Identify the preparation type.
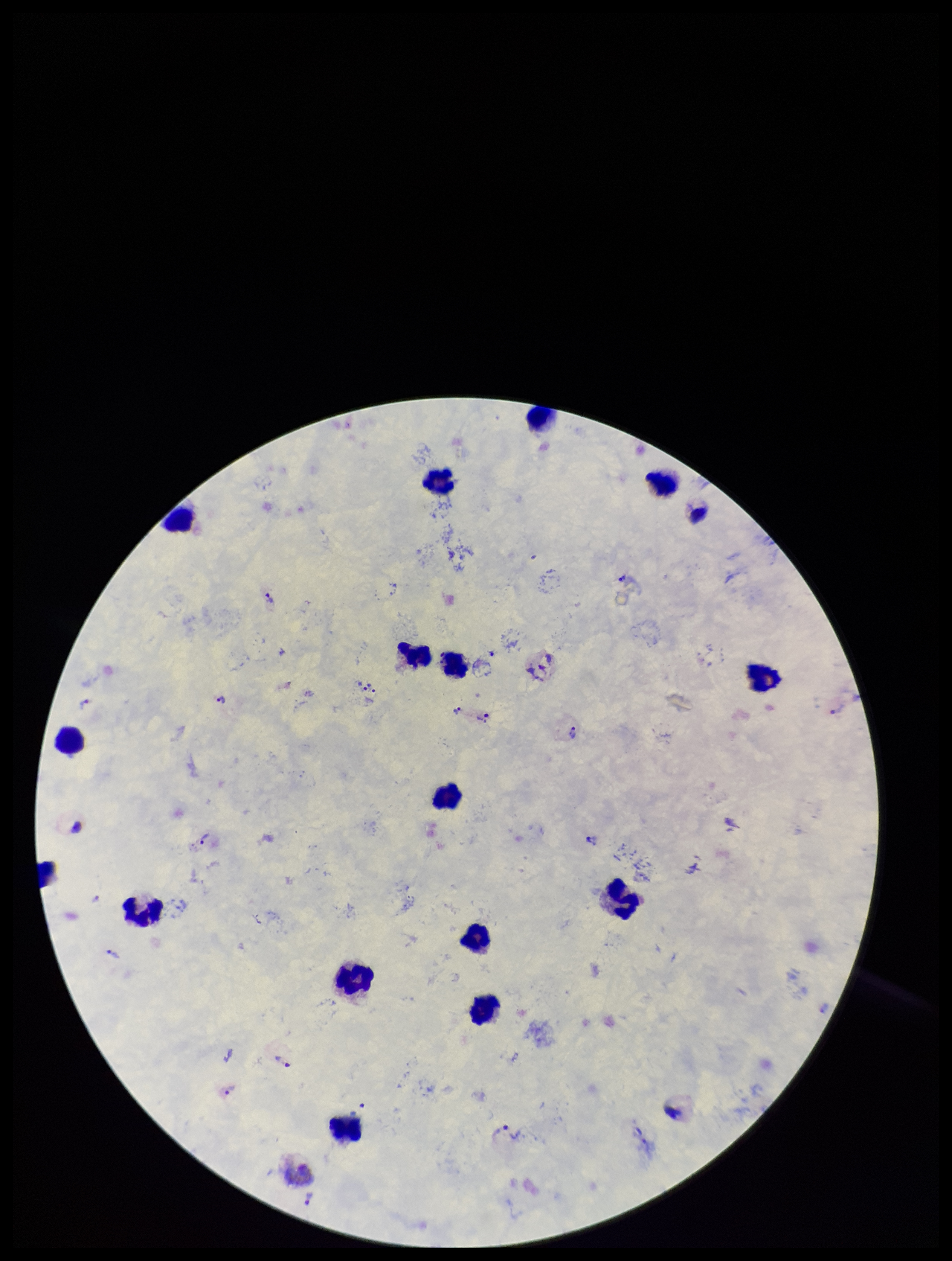
Thick.

Summary:
  - Species reported for this patient: Plasmodium vivax
  - Patient malaria status: infected
  - Capture: smartphone photograph through the microscope eyepiece
  - Parasite count: 27
  - Stain: Giemsa
  - Leukocyte count: 16
  - Image size: 952×1261 pixels
  - Plasmodium parasites: identified
  - Field of view: one from this slide